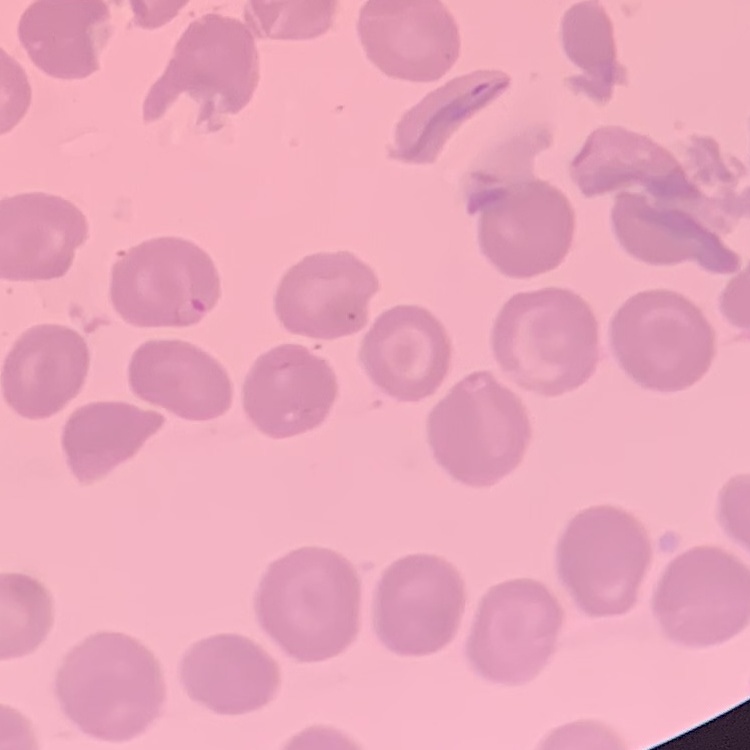

Summary:
  - Erythrocyte morphology: no rouleaux formation
  - Preparation: thin blood smear
  - Stain: Field's or Giemsa
  - Image type: one tile cut from a larger photomicrograph